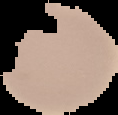
Summary:
  - Preparation: thin blood film
  - Image type: cell region segmented out of the field of view; surrounding area masked to black
  - Malaria status: uninfected
  - Image size: 118×115 pixels